Describe the morphology of the red blood cells.
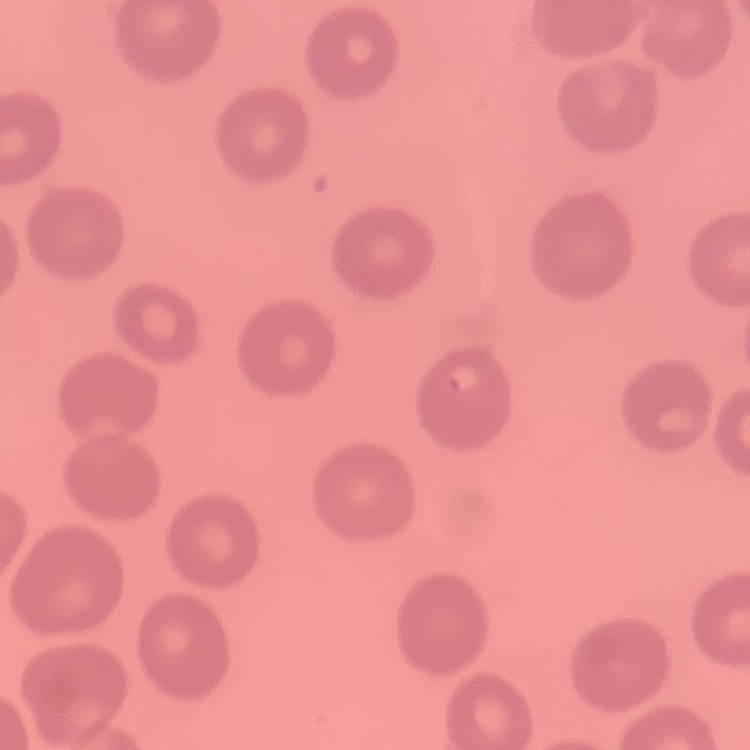

No rouleaux formation.

Thin blood smear. Field's or Giemsa stain. Square crop of a larger photomicrograph.